Name the parasite shown.
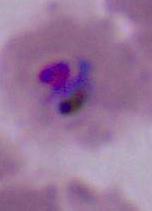
This is Plasmodium.

Summary:
  - Modality: micrograph
  - Magnification: 400x or 1000x